Name the parasite shown.
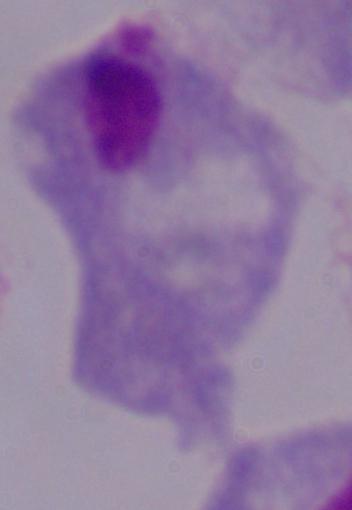
This is a trichomonad.

modality = photomicrograph
magnification = 1000x